Assess this cell for malaria.
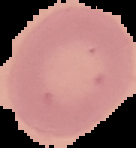
It is uninfected.

The area outside the segmented cell region is set to black. Image is 136×148 pixels. From a thin blood film.